Identify the blood parasite species.
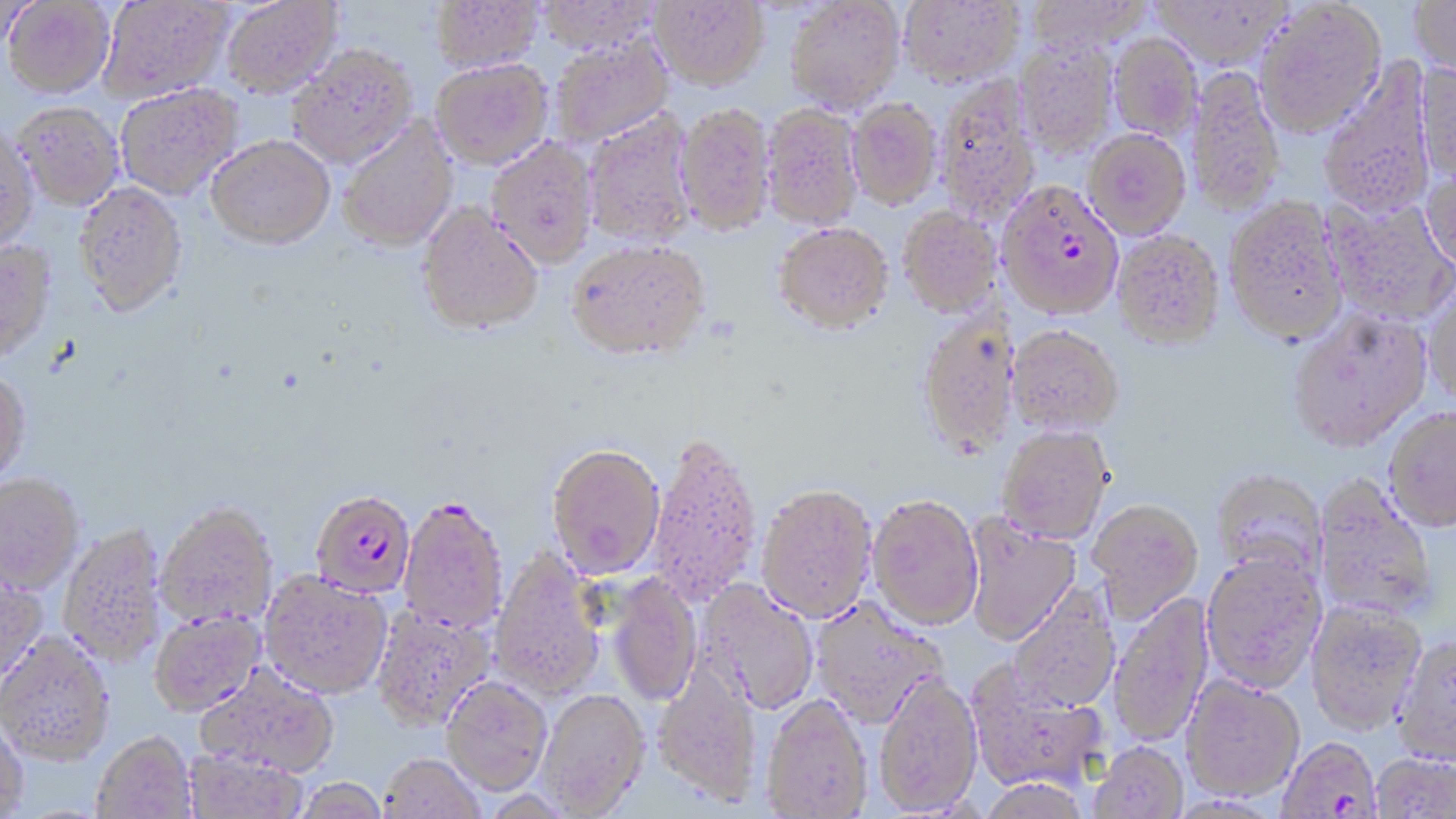
Plasmodium falciparum.

Approximate bounding boxes as (x1, y1, x2, y2) in pixels. Plasmodium falciparum-infected red blood cell locations: (997, 181, 1125, 320), (310, 489, 415, 598), (398, 495, 509, 634), (1278, 739, 1382, 818). Uninfected red blood cell locations: (3, 0, 115, 98), (99, 0, 232, 102), (222, 0, 343, 97), (535, 0, 663, 53), (785, 0, 905, 113), (899, 0, 1024, 87), (1023, 0, 1153, 53), (1410, 0, 1456, 80), (430, 1, 543, 72), (651, 1, 769, 89), (1149, 1, 1294, 66), (1254, 1, 1387, 138), (1109, 33, 1203, 139), (549, 34, 674, 147), (1015, 40, 1117, 156), (287, 44, 418, 168), (430, 58, 553, 169), (1318, 59, 1438, 219), (1416, 60, 1456, 185), (1188, 65, 1285, 216), (936, 75, 1041, 222), (114, 82, 243, 200), (847, 98, 942, 210), (14, 102, 124, 210), (675, 103, 775, 234), (762, 103, 864, 230), (583, 111, 698, 250), (337, 115, 460, 253), (0, 123, 39, 253), (1084, 128, 1191, 239), (206, 134, 335, 249), (486, 138, 599, 268), (1422, 162, 1456, 275), (73, 182, 188, 316), (1322, 195, 1456, 324), (1224, 197, 1348, 345), (415, 202, 544, 337), (898, 207, 1001, 317), (773, 223, 894, 336), (1112, 230, 1225, 350), (0, 239, 56, 360), (566, 242, 710, 366), (1423, 280, 1456, 408), (1289, 308, 1432, 452), (916, 312, 1019, 459), (1007, 325, 1125, 435), (0, 369, 31, 487), (1384, 407, 1456, 532), (997, 426, 1114, 544), (646, 433, 762, 607), (546, 447, 665, 580), (1210, 468, 1328, 585), (0, 473, 84, 593), (1312, 475, 1438, 624), (756, 485, 877, 622), (868, 494, 983, 629), (1088, 499, 1204, 621), (155, 502, 278, 629), (962, 513, 1082, 646), (59, 523, 167, 668), (489, 549, 607, 702), (1200, 551, 1327, 694), (0, 567, 47, 683), (260, 571, 392, 700), (607, 574, 703, 708), (697, 580, 820, 716), (1007, 585, 1120, 713), (1108, 593, 1214, 747), (810, 599, 947, 729), (1305, 601, 1427, 737), (371, 605, 496, 732), (149, 610, 265, 717), (0, 632, 114, 764), (1390, 636, 1456, 770), (652, 659, 762, 808), (966, 664, 1109, 795), (196, 666, 340, 779), (873, 675, 982, 816), (1180, 676, 1305, 805), (441, 677, 553, 797), (538, 691, 650, 818), (761, 694, 873, 818), (0, 713, 28, 819), (92, 732, 196, 819), (1087, 744, 1188, 819), (183, 749, 307, 818), (378, 755, 484, 818), (1370, 755, 1455, 818), (294, 779, 389, 819), (976, 780, 1093, 819). May-Grünwald-Giemsa-stained preparation. 1000x magnification. Image is 1456×819 pixels. Light microscopy. Thin blood smear. Single field of view.